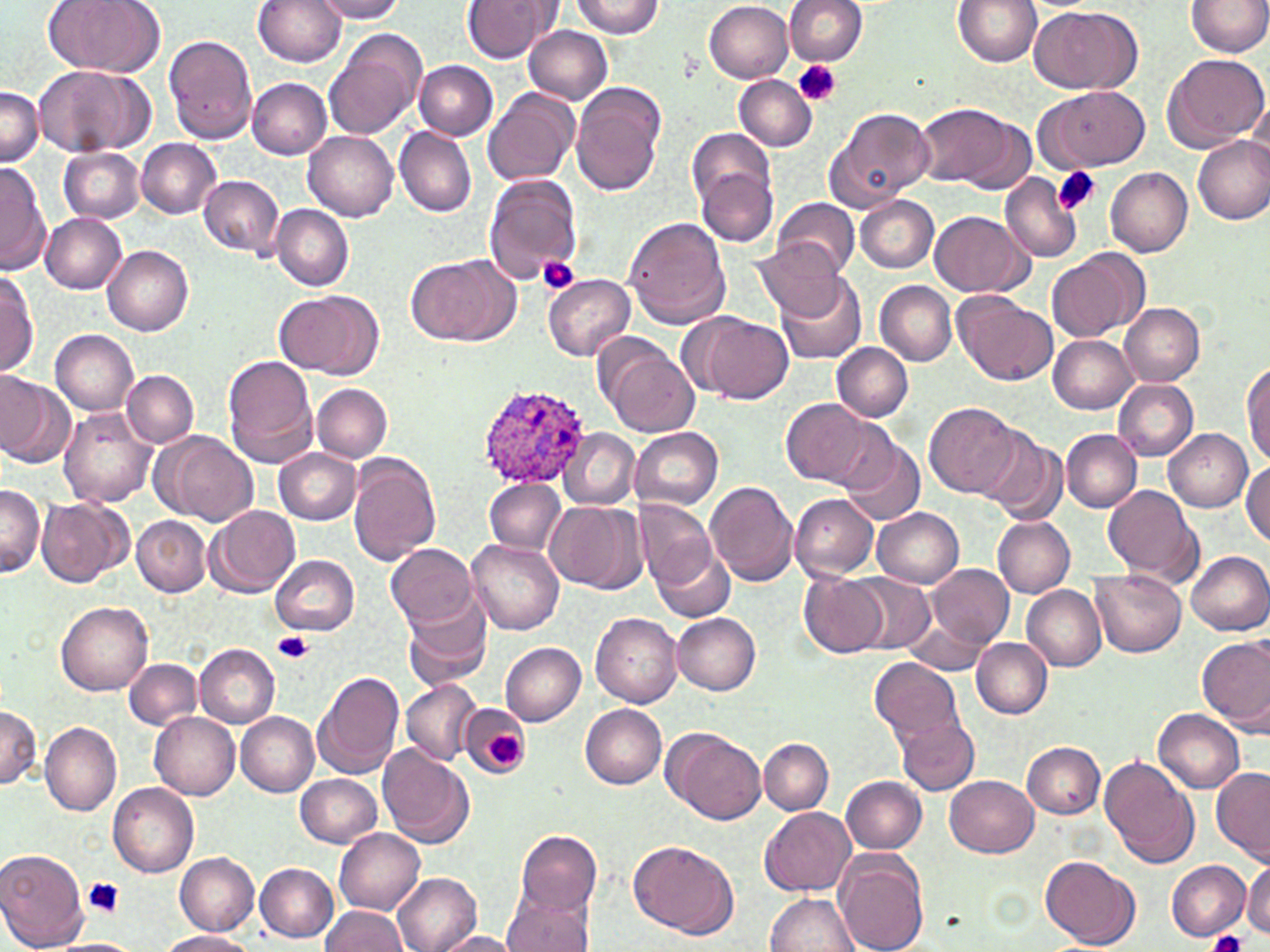

{
  "slide_level_diagnosis": "Plasmodium ovale",
  "uninfected_red_blood_cell_locations": "approximate bounding boxes as (x1, y1, x2, y2) in pixels: (44, 0, 164, 78), (254, 0, 346, 67), (312, 0, 407, 23), (571, 0, 664, 38), (783, 0, 867, 66), (953, 0, 1041, 67), (1186, 0, 1270, 58), (460, 1, 558, 63), (705, 1, 794, 83), (1030, 6, 1144, 95), (524, 25, 612, 104), (322, 29, 426, 141), (164, 34, 256, 143), (1160, 52, 1270, 153), (415, 61, 498, 140), (34, 65, 150, 159), (733, 76, 816, 151), (247, 78, 333, 160), (570, 82, 666, 196), (1035, 85, 1149, 173), (483, 86, 581, 187), (0, 87, 42, 165), (1248, 91, 1270, 175), (915, 102, 1025, 191), (823, 106, 936, 212), (394, 126, 476, 217), (304, 131, 398, 222), (1193, 137, 1270, 225), (137, 138, 221, 218), (58, 146, 145, 223), (693, 156, 780, 248), (0, 163, 48, 276), (1106, 167, 1193, 257), (483, 174, 582, 284), (1000, 174, 1082, 262), (198, 175, 284, 257), (855, 195, 939, 272), (773, 199, 860, 279), (271, 205, 352, 291), (930, 211, 1031, 296), (40, 213, 128, 293), (623, 217, 732, 330), (755, 242, 845, 319), (103, 245, 193, 336), (1046, 248, 1151, 345), (407, 253, 521, 347), (0, 269, 38, 376), (543, 274, 636, 360), (779, 275, 868, 365), (876, 281, 956, 366), (273, 289, 382, 379), (955, 295, 1056, 385), (1118, 303, 1206, 386), (687, 312, 794, 404), (49, 328, 138, 414), (1048, 334, 1139, 414), (597, 338, 698, 437), (831, 343, 912, 420), (222, 355, 318, 464), (1242, 361, 1270, 465), (122, 371, 199, 447), (0, 374, 75, 468), (1113, 378, 1199, 461), (313, 383, 392, 463), (779, 399, 883, 489), (924, 401, 1023, 499), (58, 408, 155, 508), (630, 428, 723, 510), (560, 429, 639, 511), (1164, 429, 1253, 512), (839, 430, 925, 526), (981, 430, 1068, 525), (1061, 430, 1143, 512), (151, 431, 258, 526), (274, 448, 362, 524), (347, 454, 440, 564), (1242, 460, 1270, 547), (484, 479, 567, 553), (706, 481, 799, 585), (1101, 484, 1202, 586), (0, 485, 44, 579), (788, 492, 878, 580), (37, 496, 132, 588), (634, 499, 715, 589), (546, 501, 648, 594), (205, 505, 302, 598), (871, 506, 964, 588), (132, 516, 210, 596), (994, 517, 1075, 597), (467, 538, 564, 636), (385, 543, 478, 629), (652, 544, 734, 624), (1188, 551, 1270, 634), (268, 553, 360, 635), (927, 563, 1014, 650), (1091, 568, 1186, 657), (799, 572, 891, 658), (847, 573, 935, 653), (1022, 585, 1107, 670), (401, 596, 493, 691), (56, 599, 153, 695), (672, 613, 761, 695), (592, 614, 682, 708), (902, 616, 988, 674), (1197, 636, 1270, 734), (972, 638, 1052, 718), (500, 642, 586, 726), (195, 644, 279, 727), (870, 657, 964, 747), (124, 658, 202, 730), (313, 670, 404, 780), (402, 680, 480, 765), (0, 702, 39, 789), (461, 704, 529, 779), (580, 705, 667, 788), (1154, 709, 1245, 793), (150, 712, 241, 800), (236, 713, 319, 796), (898, 716, 979, 794), (41, 722, 122, 816), (663, 727, 766, 825), (759, 738, 835, 814), (1022, 742, 1104, 818), (377, 744, 474, 848), (1100, 757, 1202, 870), (1212, 769, 1269, 865), (296, 773, 382, 848), (945, 774, 1038, 857), (841, 775, 928, 854), (108, 781, 200, 878), (758, 806, 856, 896), (335, 827, 424, 913), (515, 828, 603, 920), (629, 841, 738, 938), (0, 845, 87, 951), (833, 850, 929, 952), (173, 853, 260, 936), (1040, 853, 1140, 949), (1166, 860, 1252, 941), (255, 861, 338, 940), (1243, 861, 1270, 937), (392, 873, 483, 952), (501, 884, 597, 952), (766, 892, 862, 951), (320, 905, 408, 952), (160, 930, 253, 952), (430, 931, 529, 951), (50, 940, 144, 952)",
  "magnification": "1000x",
  "platelet_locations": "approximate bounding boxes as (x1, y1, x2, y2) in pixels: (792, 59, 840, 107), (1054, 166, 1101, 217), (537, 255, 581, 295), (273, 630, 314, 664), (487, 734, 526, 768), (85, 877, 124, 917), (1209, 931, 1246, 952)",
  "preparation": "thin blood film",
  "modality": "light microscopy",
  "plasmodium_ovale_infected_red_blood_cell_locations": "approximate bounding boxes as (x1, y1, x2, y2) in pixels: (477, 384, 591, 490)",
  "stain": "May-Grünwald-Giemsa",
  "field_of_view": "one of a larger specimen",
  "image_size": "1270×952 pixels"
}